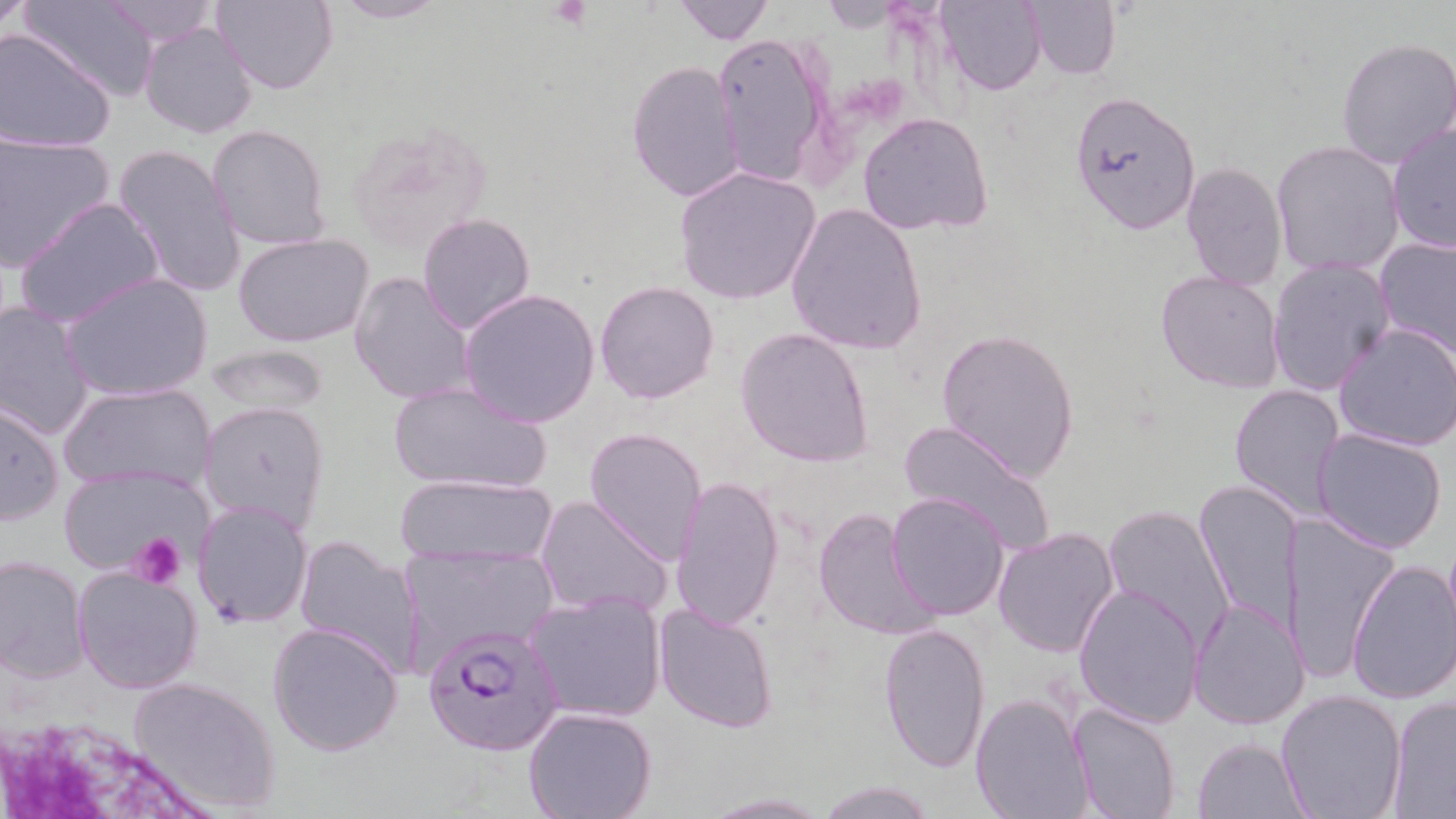
{
  "slide_level_diagnosis": "Plasmodium falciparum",
  "preparation": "thin blood smear",
  "uninfected_red_blood_cell_locations": "approximate bounding boxes as named x1/y1/x2/y2 corners in pixels: (x1=0, y1=0, x2=35, y2=38), (x1=210, y1=0, x2=338, y2=93), (x1=323, y1=0, x2=451, y2=24), (x1=672, y1=0, x2=775, y2=44), (x1=937, y1=0, x2=1048, y2=94), (x1=1024, y1=0, x2=1119, y2=81), (x1=20, y1=1, x2=160, y2=104), (x1=101, y1=1, x2=223, y2=49), (x1=140, y1=21, x2=258, y2=139), (x1=0, y1=28, x2=118, y2=152), (x1=711, y1=30, x2=833, y2=190), (x1=1336, y1=38, x2=1455, y2=169), (x1=626, y1=61, x2=746, y2=202), (x1=1070, y1=90, x2=1200, y2=231), (x1=858, y1=112, x2=994, y2=236), (x1=1387, y1=120, x2=1456, y2=253), (x1=207, y1=125, x2=331, y2=249), (x1=0, y1=133, x2=117, y2=272), (x1=1272, y1=141, x2=1405, y2=276), (x1=112, y1=143, x2=245, y2=299), (x1=1181, y1=162, x2=1286, y2=291), (x1=674, y1=166, x2=819, y2=306), (x1=16, y1=198, x2=166, y2=329), (x1=786, y1=202, x2=927, y2=355), (x1=417, y1=212, x2=536, y2=336), (x1=234, y1=235, x2=373, y2=349), (x1=1374, y1=237, x2=1456, y2=359), (x1=1268, y1=257, x2=1396, y2=399), (x1=1155, y1=271, x2=1284, y2=393), (x1=60, y1=273, x2=214, y2=403), (x1=348, y1=273, x2=477, y2=406), (x1=595, y1=279, x2=721, y2=404), (x1=457, y1=288, x2=600, y2=429), (x1=0, y1=300, x2=97, y2=441), (x1=1334, y1=322, x2=1456, y2=451), (x1=735, y1=327, x2=875, y2=468), (x1=934, y1=328, x2=1081, y2=481), (x1=202, y1=343, x2=330, y2=418), (x1=386, y1=379, x2=551, y2=495), (x1=61, y1=382, x2=213, y2=496), (x1=1229, y1=382, x2=1346, y2=520), (x1=1, y1=400, x2=65, y2=526), (x1=199, y1=401, x2=329, y2=533), (x1=898, y1=420, x2=1056, y2=552), (x1=583, y1=426, x2=707, y2=563), (x1=1312, y1=427, x2=1448, y2=554), (x1=58, y1=464, x2=208, y2=580), (x1=399, y1=475, x2=557, y2=564), (x1=670, y1=475, x2=784, y2=631), (x1=1194, y1=478, x2=1303, y2=637), (x1=886, y1=492, x2=1009, y2=619), (x1=535, y1=495, x2=673, y2=620), (x1=192, y1=500, x2=312, y2=628), (x1=1101, y1=504, x2=1236, y2=651), (x1=813, y1=505, x2=939, y2=642), (x1=1280, y1=513, x2=1401, y2=688), (x1=992, y1=526, x2=1120, y2=658), (x1=292, y1=535, x2=429, y2=678), (x1=397, y1=544, x2=559, y2=668), (x1=0, y1=556, x2=91, y2=684), (x1=1345, y1=558, x2=1456, y2=706), (x1=72, y1=564, x2=203, y2=695), (x1=1073, y1=583, x2=1205, y2=726), (x1=524, y1=589, x2=666, y2=723), (x1=1187, y1=596, x2=1310, y2=730), (x1=653, y1=602, x2=778, y2=734), (x1=268, y1=621, x2=404, y2=758), (x1=878, y1=622, x2=990, y2=771), (x1=126, y1=675, x2=279, y2=814), (x1=1275, y1=687, x2=1407, y2=819), (x1=971, y1=692, x2=1095, y2=818), (x1=1386, y1=698, x2=1456, y2=817), (x1=1069, y1=702, x2=1180, y2=819), (x1=524, y1=705, x2=656, y2=819), (x1=1193, y1=736, x2=1310, y2=817), (x1=815, y1=779, x2=936, y2=818), (x1=698, y1=793, x2=830, y2=818)",
  "plasmodium_falciparum_infected_red_blood_cell_locations": "approximate bounding boxes as named x1/y1/x2/y2 corners in pixels: (x1=423, y1=622, x2=565, y2=758)",
  "image_size": "1456×819 pixels",
  "stain": "May-Grünwald-Giemsa",
  "platelet_locations": "approximate bounding boxes as named x1/y1/x2/y2 corners in pixels: (x1=546, y1=1, x2=594, y2=29), (x1=130, y1=531, x2=186, y2=589)",
  "magnification": "1000x",
  "field_of_view": "one of a larger specimen",
  "modality": "optical microscopy"
}